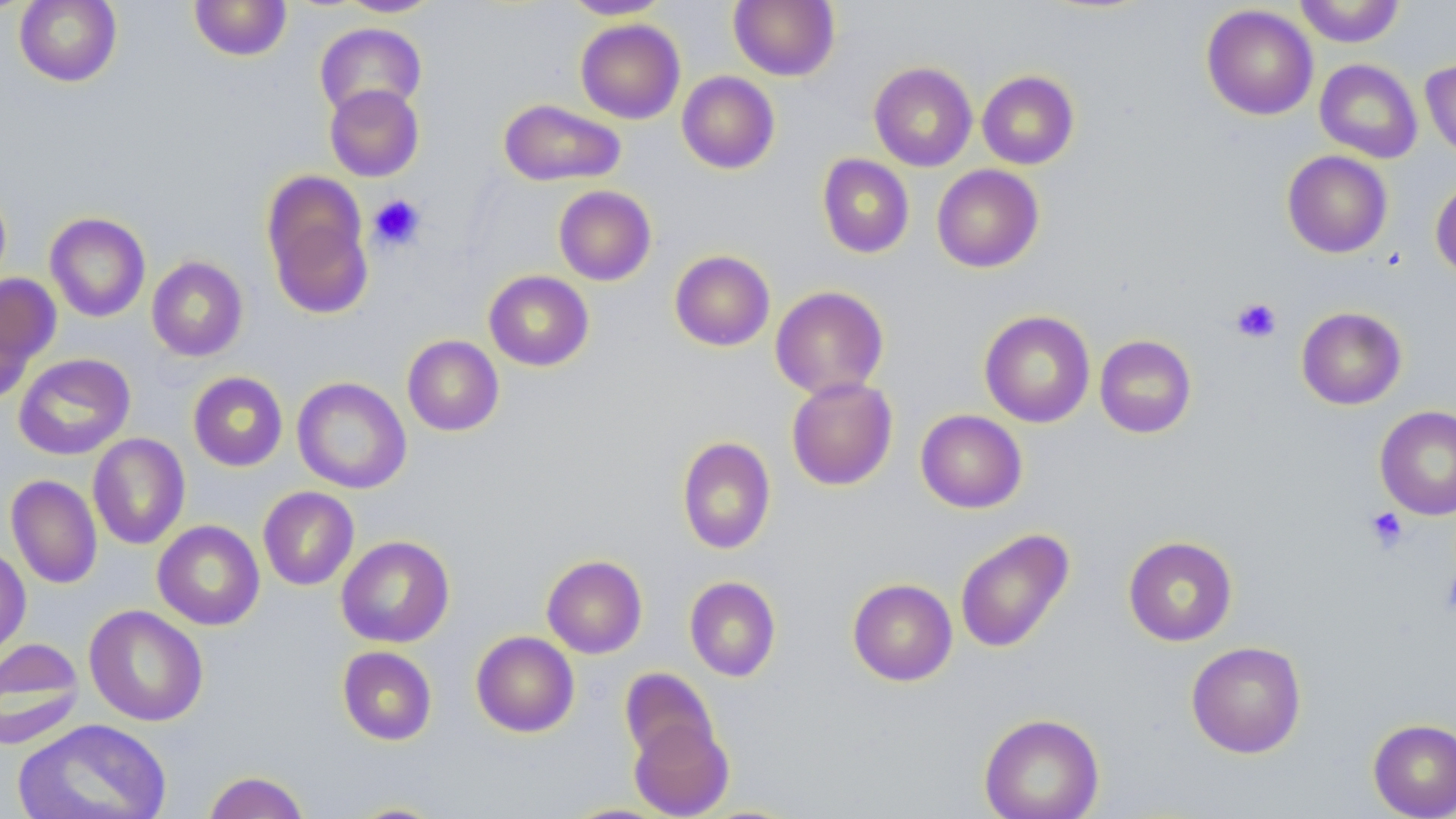

Summary:
  - Coordinate format: approximate bounding boxes as (x1, y1, x2, y2) in pixels
  - Platelet locations: (369, 194, 426, 251), (1230, 297, 1282, 344), (1365, 506, 1408, 552), (1440, 569, 1456, 616)
  - Uninfected red blood cell locations: (0, 0, 29, 17), (14, 0, 122, 87), (189, 0, 293, 61), (336, 0, 442, 17), (562, 0, 672, 19), (728, 0, 840, 81), (1293, 0, 1406, 47), (1201, 4, 1318, 120), (575, 19, 685, 124), (315, 22, 426, 119), (1315, 59, 1423, 163), (1420, 59, 1456, 161), (869, 62, 977, 172), (977, 70, 1079, 169), (677, 71, 780, 174), (324, 84, 424, 181), (498, 99, 626, 187), (1282, 150, 1393, 258), (817, 154, 914, 258), (931, 164, 1044, 273), (261, 171, 374, 317), (1430, 176, 1456, 281), (553, 185, 657, 286), (45, 213, 150, 322), (669, 250, 775, 351), (146, 256, 248, 361), (483, 270, 594, 371), (0, 273, 60, 396), (770, 286, 889, 400), (1296, 306, 1407, 410), (979, 310, 1095, 427), (1095, 334, 1197, 438), (402, 335, 504, 436), (13, 353, 135, 460), (188, 371, 288, 471), (292, 376, 411, 494), (786, 376, 898, 491), (1374, 405, 1456, 520), (915, 409, 1027, 513), (88, 433, 190, 550), (677, 436, 776, 554), (6, 475, 102, 589), (258, 486, 359, 590), (152, 520, 265, 630), (954, 528, 1074, 653), (336, 535, 454, 648), (1123, 536, 1238, 646), (0, 544, 31, 663), (542, 555, 648, 658), (684, 576, 781, 682), (847, 578, 958, 686), (84, 604, 208, 726), (471, 631, 579, 738), (0, 637, 85, 749), (1186, 641, 1307, 758), (337, 646, 437, 745), (620, 667, 718, 766), (979, 713, 1105, 819), (12, 718, 173, 819), (1367, 718, 1456, 818), (629, 719, 733, 818), (203, 771, 309, 819), (341, 801, 450, 818)
  - Slide-level diagnosis: negative for blood parasites
  - Image size: 1456×819 pixels
  - Field of view: one of a larger specimen
  - Magnification: 1000x
  - Modality: optical microscopy
  - Stain: May-Grünwald-Giemsa
  - Preparation: thin blood smear